Locate every blood parasite and identify its species.
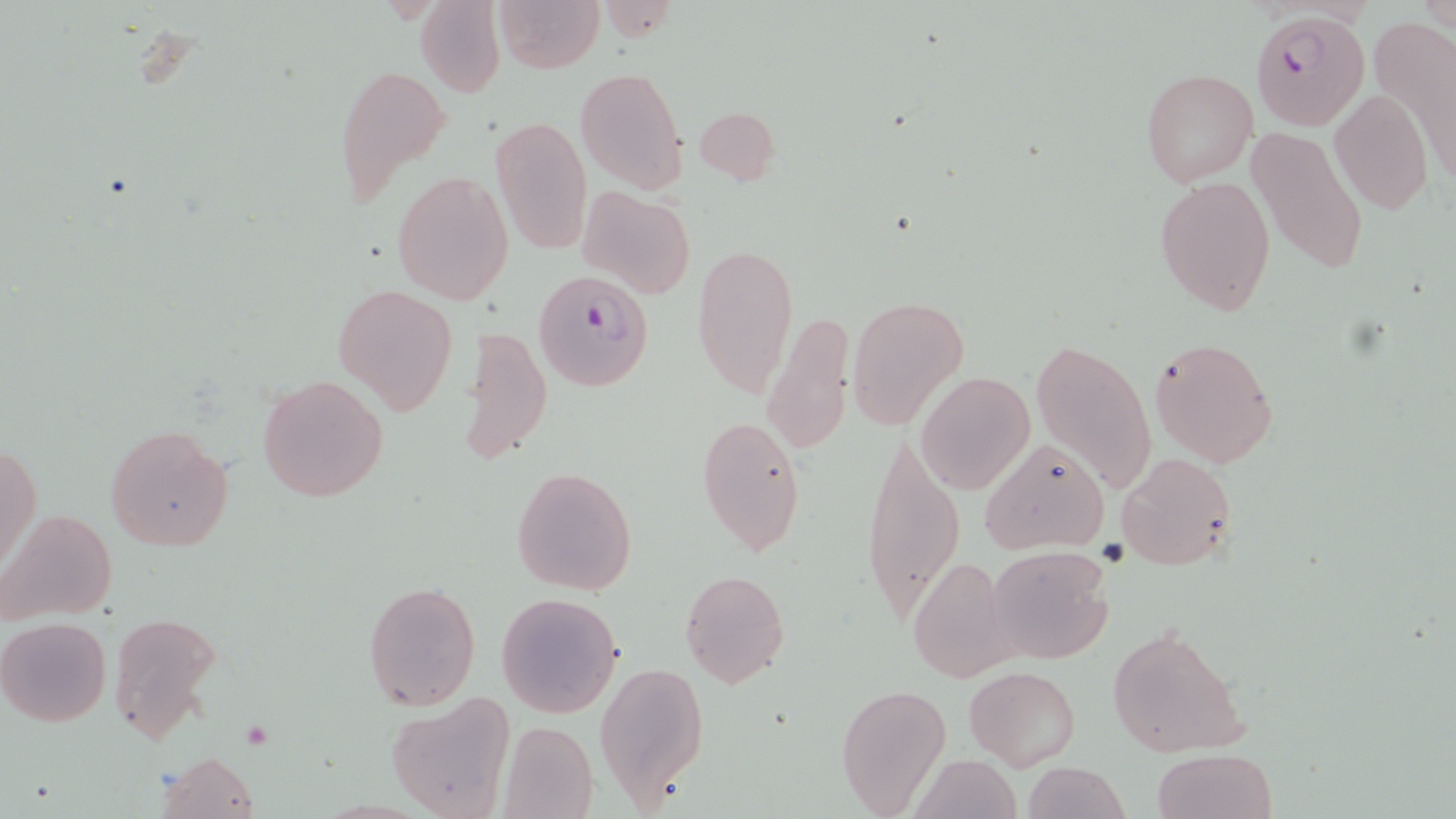

Approximate bounding boxes as [x1, y1, x2, y2] in pixels.
Plasmodium falciparum-infected red blood cells: [1250, 9, 1370, 131], [533, 270, 654, 391].
No Plasmodium ovale, Plasmodium malariae, Plasmodium vivax, Babesia divergens, or Trypanosoma brucei observed.

Uninfected red blood cell locations: [493, 0, 604, 73], [417, 1, 504, 97], [592, 3, 682, 41], [1372, 17, 1456, 183], [332, 62, 447, 205], [575, 67, 686, 192], [1140, 68, 1257, 188], [1329, 90, 1433, 214], [693, 105, 781, 185], [488, 115, 593, 254], [1248, 127, 1368, 277], [392, 170, 513, 305], [1154, 174, 1275, 314], [578, 185, 693, 300], [691, 242, 799, 399], [331, 284, 459, 413], [847, 295, 968, 432], [762, 309, 855, 457], [464, 323, 553, 466], [1029, 335, 1159, 498], [1148, 335, 1279, 467], [917, 372, 1035, 494], [257, 375, 388, 502], [696, 415, 807, 554], [104, 423, 234, 552], [862, 430, 964, 623], [979, 437, 1109, 555], [1, 443, 41, 574], [1116, 451, 1236, 569], [510, 465, 638, 595], [0, 507, 117, 627], [985, 545, 1114, 664], [907, 554, 1019, 684], [679, 569, 790, 689], [362, 581, 481, 710], [496, 592, 622, 719], [108, 609, 224, 746], [0, 616, 111, 727], [1105, 621, 1248, 757], [594, 659, 708, 806], [964, 664, 1081, 769], [836, 682, 952, 816], [386, 695, 515, 819], [499, 720, 597, 819], [1150, 748, 1278, 819], [158, 751, 260, 819], [910, 753, 1022, 819], [1019, 761, 1130, 819]. Slide-level diagnosis: Plasmodium falciparum. 1000x magnification. Single field of view. Light microscopy. May-Grünwald-Giemsa-stained preparation. Image is 1456×819 pixels. Thin blood smear.